Outline each blood parasite and name the species.
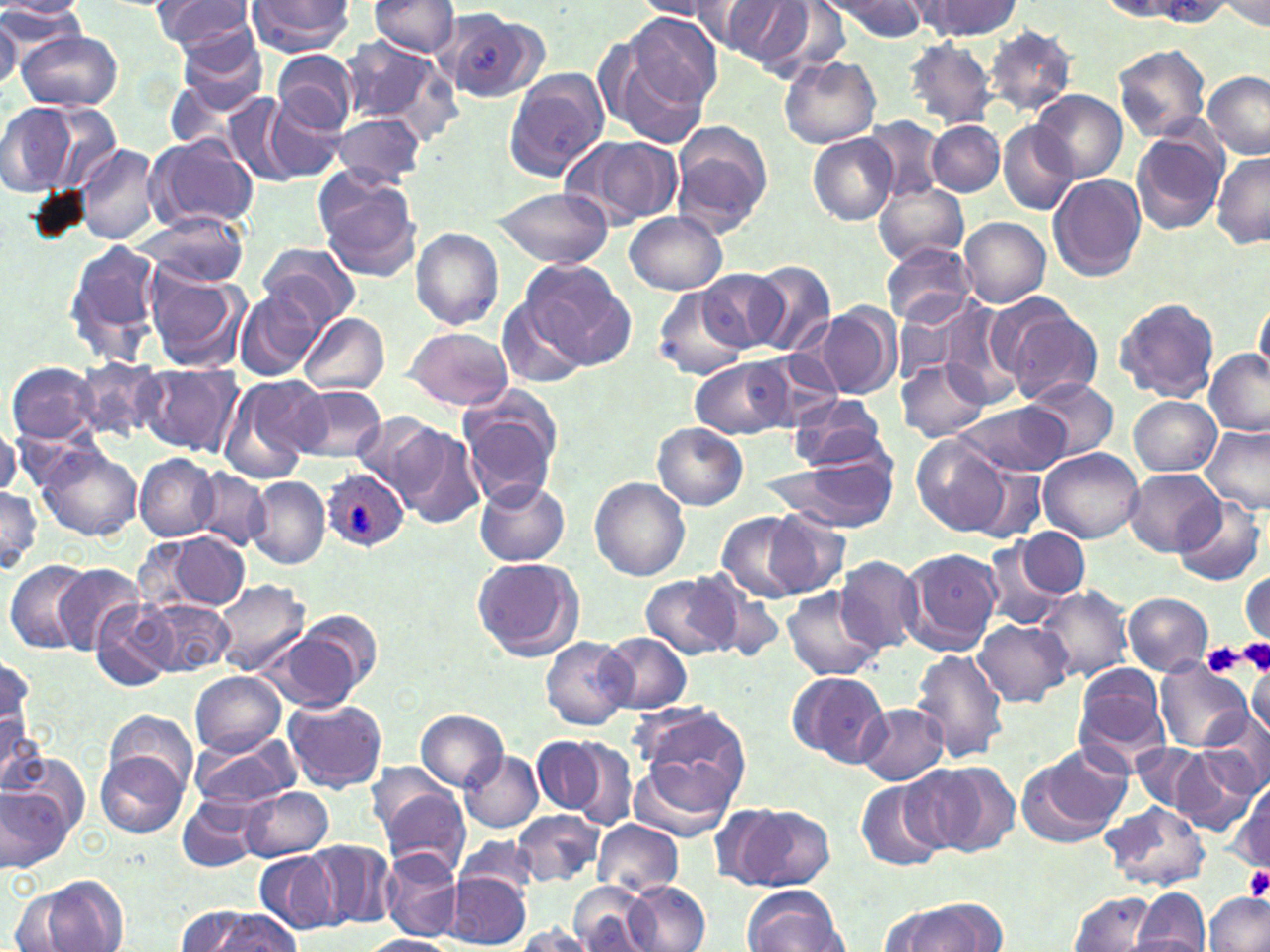

Approximate bounding boxes as (x1,y1)-(x2,y2) corner pairs in pixels.
Plasmodium ovale-infected red blood cells: (322,469)-(408,550).
No Plasmodium falciparum, Plasmodium malariae, Plasmodium vivax, Babesia divergens, or Trypanosoma brucei observed.

Summary:
  - Uninfected red blood cell locations: (149,0)-(257,56), (367,0)-(461,58), (633,0)-(723,19), (825,0)-(931,40), (0,1)-(91,24), (244,1)-(354,54), (703,1)-(815,66), (912,1)-(1018,41), (1216,1)-(1269,31), (678,2)-(778,48), (0,5)-(88,56), (444,12)-(547,104), (622,13)-(723,115), (0,16)-(22,95), (983,25)-(1077,116), (173,26)-(270,119), (16,30)-(122,111), (341,35)-(441,123), (603,37)-(713,153), (905,39)-(998,129), (1113,45)-(1212,142), (273,49)-(359,135), (780,54)-(881,150), (505,69)-(610,181), (1202,71)-(1269,160), (1029,90)-(1126,183), (223,92)-(299,186), (265,98)-(346,182), (0,100)-(87,196), (31,101)-(123,197), (332,113)-(426,189), (862,117)-(947,201), (927,120)-(1004,196), (998,120)-(1077,216), (669,121)-(772,233), (1130,130)-(1226,234), (146,134)-(259,232), (809,135)-(898,225), (572,136)-(682,229), (77,144)-(160,247), (1211,152)-(1270,248), (315,171)-(422,280), (1048,175)-(1146,281), (873,181)-(971,266), (489,187)-(613,267), (623,210)-(729,294), (138,211)-(251,289), (960,217)-(1051,307), (411,228)-(503,330), (64,238)-(163,364), (259,243)-(361,330), (882,244)-(976,328), (522,257)-(636,367), (745,260)-(835,357), (141,265)-(248,373), (696,268)-(785,352), (235,288)-(323,381), (655,290)-(752,380), (1254,294)-(1269,385), (497,296)-(590,390), (1114,296)-(1219,403), (891,300)-(986,387), (819,303)-(900,399), (936,303)-(1024,405), (1005,308)-(1104,406), (299,313)-(389,396), (406,327)-(513,410), (1203,349)-(1269,435), (690,356)-(798,438), (72,357)-(164,442), (897,360)-(989,442), (7,361)-(98,444), (136,364)-(242,456), (219,375)-(327,480), (1028,379)-(1117,462), (289,383)-(388,464), (787,394)-(889,473), (1129,395)-(1218,476), (459,396)-(562,505), (958,400)-(1073,477), (352,410)-(448,504), (391,423)-(486,528), (652,423)-(748,511), (1202,426)-(1270,513), (912,436)-(1011,536), (33,441)-(142,542), (1038,448)-(1144,544), (765,450)-(899,533), (135,454)-(219,541), (965,460)-(1047,545), (1120,469)-(1225,557), (190,470)-(271,552), (247,477)-(329,567), (590,477)-(691,580), (475,480)-(569,567), (0,487)-(42,573), (1172,496)-(1265,588), (762,510)-(852,598), (716,511)-(812,602), (1018,527)-(1089,599), (158,533)-(252,613), (980,541)-(1065,632), (899,547)-(1003,655), (471,556)-(584,662), (837,556)-(923,653), (7,560)-(94,655), (51,564)-(144,654), (640,572)-(743,659), (1241,572)-(1269,641), (212,578)-(309,674), (1035,585)-(1135,686), (781,586)-(885,681), (1123,593)-(1213,675), (90,598)-(178,691), (142,599)-(235,676), (974,618)-(1070,707), (257,621)-(374,715), (597,633)-(693,714), (541,637)-(633,730), (910,648)-(1009,765), (1,658)-(34,749), (1153,661)-(1252,751), (1074,663)-(1170,759), (1247,667)-(1269,738), (786,670)-(889,767), (190,671)-(286,756), (283,697)-(387,793), (630,699)-(750,791), (854,703)-(948,785), (416,709)-(509,792), (104,710)-(196,794), (1201,710)-(1270,801), (0,712)-(45,794), (190,731)-(299,811), (532,734)-(609,818), (561,738)-(642,831), (1132,743)-(1203,810), (1015,747)-(1131,849), (1171,747)-(1258,834), (96,751)-(188,837), (460,751)-(543,833), (627,755)-(737,844), (0,759)-(81,869), (912,763)-(1014,856), (854,777)-(947,872), (1229,783)-(1269,874), (240,786)-(334,861), (377,787)-(470,879), (177,796)-(261,873), (1103,801)-(1210,890), (725,802)-(833,890), (512,810)-(605,886), (591,820)-(684,896), (456,836)-(541,901), (308,839)-(395,929), (253,849)-(342,937), (379,851)-(464,942), (447,871)-(531,948), (28,876)-(128,952), (626,880)-(710,951), (568,883)-(659,952), (742,886)-(848,952), (1132,887)-(1211,952), (10,890)-(86,952), (1069,891)-(1157,950), (1202,892)-(1269,952), (886,902)-(1001,951), (173,905)-(257,952), (197,911)-(303,952), (512,925)-(595,951), (364,934)-(456,952)
  - Platelet locations: (1237,636)-(1270,675), (1202,642)-(1246,676), (1243,866)-(1270,902)
  - Slide-level diagnosis: Plasmodium ovale
  - Preparation: thin blood film
  - Modality: light microscopy
  - Stain: May-Grünwald-Giemsa
  - Field of view: single
  - Magnification: 1000x
  - Image size: 1270×952 pixels